Give the extent of all Plasmodium vivax-infected red blood cells.
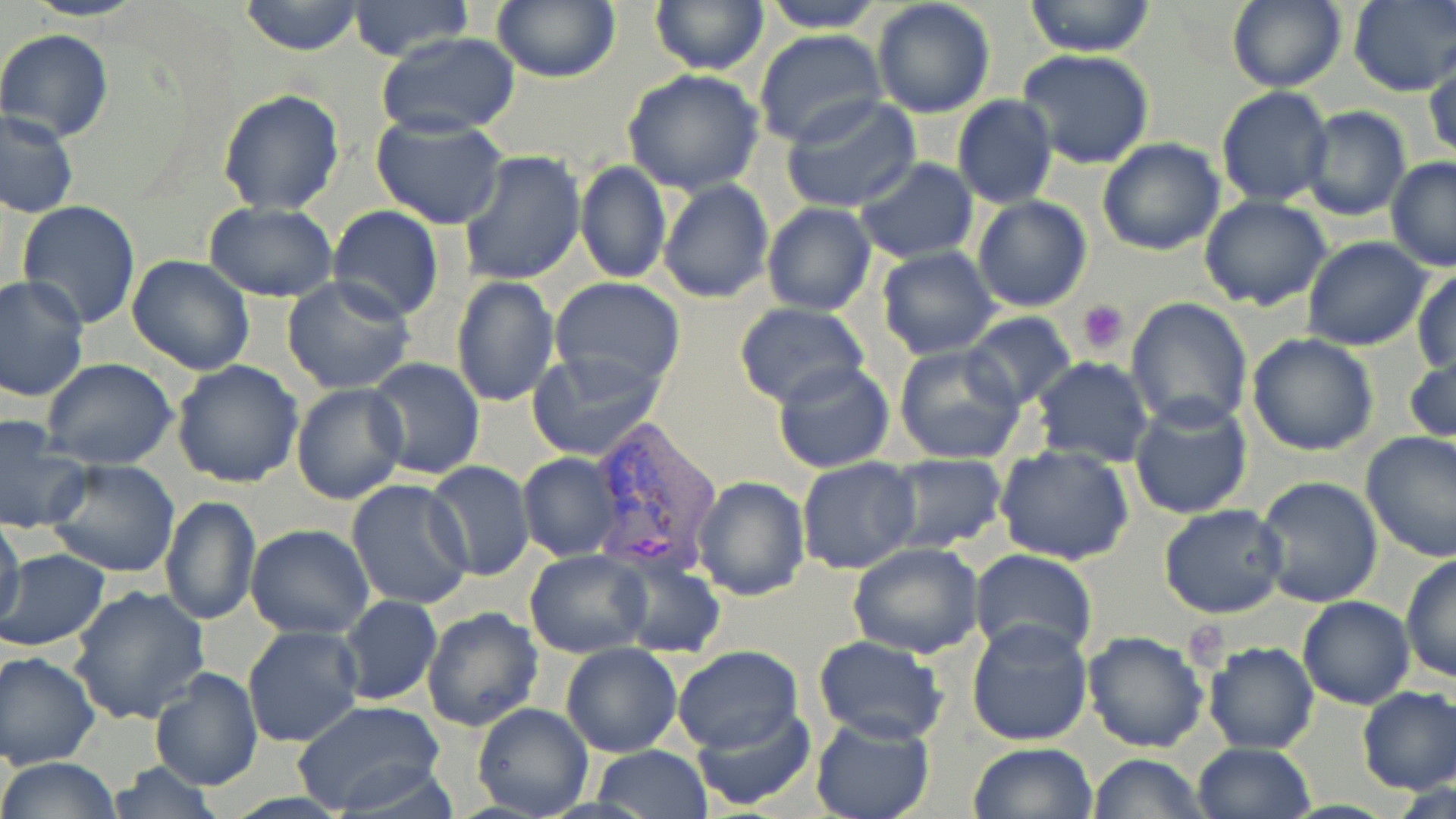

Approximate bounding boxes as [x1, y1, x2, y2] in pixels.
Plasmodium vivax-infected red blood cells: [587, 421, 724, 581].

{
  "slide_level_diagnosis": "Plasmodium vivax",
  "uninfected_red_blood_cell_locations": "approximate bounding boxes as [x1, y1, x2, y2] in pixels: [240, 0, 365, 56], [491, 0, 621, 84], [648, 0, 768, 74], [758, 0, 886, 32], [871, 0, 996, 119], [1023, 0, 1158, 56], [1226, 0, 1347, 93], [1349, 0, 1455, 94], [346, 1, 476, 63], [0, 28, 113, 142], [754, 31, 887, 148], [374, 33, 524, 136], [1016, 51, 1155, 170], [1426, 59, 1456, 161], [622, 70, 767, 194], [1215, 86, 1333, 207], [216, 88, 346, 215], [781, 95, 921, 213], [952, 96, 1059, 209], [1300, 106, 1412, 221], [1, 110, 78, 219], [370, 115, 508, 229], [1097, 138, 1226, 257], [458, 150, 587, 286], [854, 158, 978, 263], [1386, 158, 1456, 272], [574, 159, 671, 285], [657, 178, 774, 304], [972, 195, 1093, 313], [1198, 196, 1332, 311], [15, 200, 141, 330], [205, 202, 337, 302], [761, 202, 877, 316], [328, 205, 444, 322], [1303, 237, 1433, 350], [876, 247, 1000, 360], [127, 255, 255, 375], [1412, 266, 1456, 376], [0, 275, 90, 402], [282, 276, 417, 396], [449, 276, 561, 408], [547, 276, 686, 395], [1126, 297, 1254, 430], [734, 302, 870, 409], [961, 311, 1078, 410], [1247, 333, 1380, 457], [893, 342, 1026, 465], [1405, 344, 1456, 448], [526, 349, 665, 461], [1032, 356, 1155, 467], [365, 358, 484, 480], [42, 359, 179, 470], [172, 359, 305, 487], [770, 359, 896, 475], [291, 383, 408, 505], [1128, 397, 1253, 521], [0, 413, 88, 536], [1360, 431, 1456, 561], [993, 445, 1136, 567], [517, 452, 621, 561], [882, 454, 1008, 552], [796, 456, 921, 574], [42, 457, 180, 580], [425, 461, 535, 583], [693, 475, 812, 603], [1255, 477, 1384, 609], [347, 480, 474, 611], [159, 495, 262, 627], [1159, 504, 1289, 618], [1, 516, 23, 630], [246, 525, 374, 639], [846, 543, 986, 659], [1, 548, 109, 651], [969, 548, 1097, 665], [525, 549, 653, 658], [614, 551, 726, 658], [1400, 552, 1455, 684], [68, 585, 210, 726], [338, 596, 442, 706], [1298, 596, 1414, 708], [421, 606, 545, 732], [966, 617, 1093, 746], [241, 626, 363, 748], [1083, 631, 1209, 752], [812, 636, 949, 745], [560, 641, 682, 758], [1203, 641, 1319, 754], [671, 645, 802, 753], [0, 650, 100, 768], [149, 666, 263, 789], [1356, 686, 1456, 795], [294, 700, 447, 818], [472, 702, 593, 819], [693, 702, 816, 810], [808, 713, 935, 819], [1191, 742, 1315, 819], [969, 743, 1097, 819], [589, 746, 713, 819], [1089, 753, 1207, 819], [0, 757, 122, 818], [104, 761, 226, 819]",
  "magnification": "1000x",
  "preparation": "thin blood film",
  "image_size": "1456×819 pixels",
  "platelet_locations": "approximate bounding boxes as [x1, y1, x2, y2] in pixels: [1078, 300, 1130, 352]",
  "field_of_view": "single",
  "stain": "May-Grünwald-Giemsa",
  "modality": "optical microscopy"
}